Name the blood parasite species.
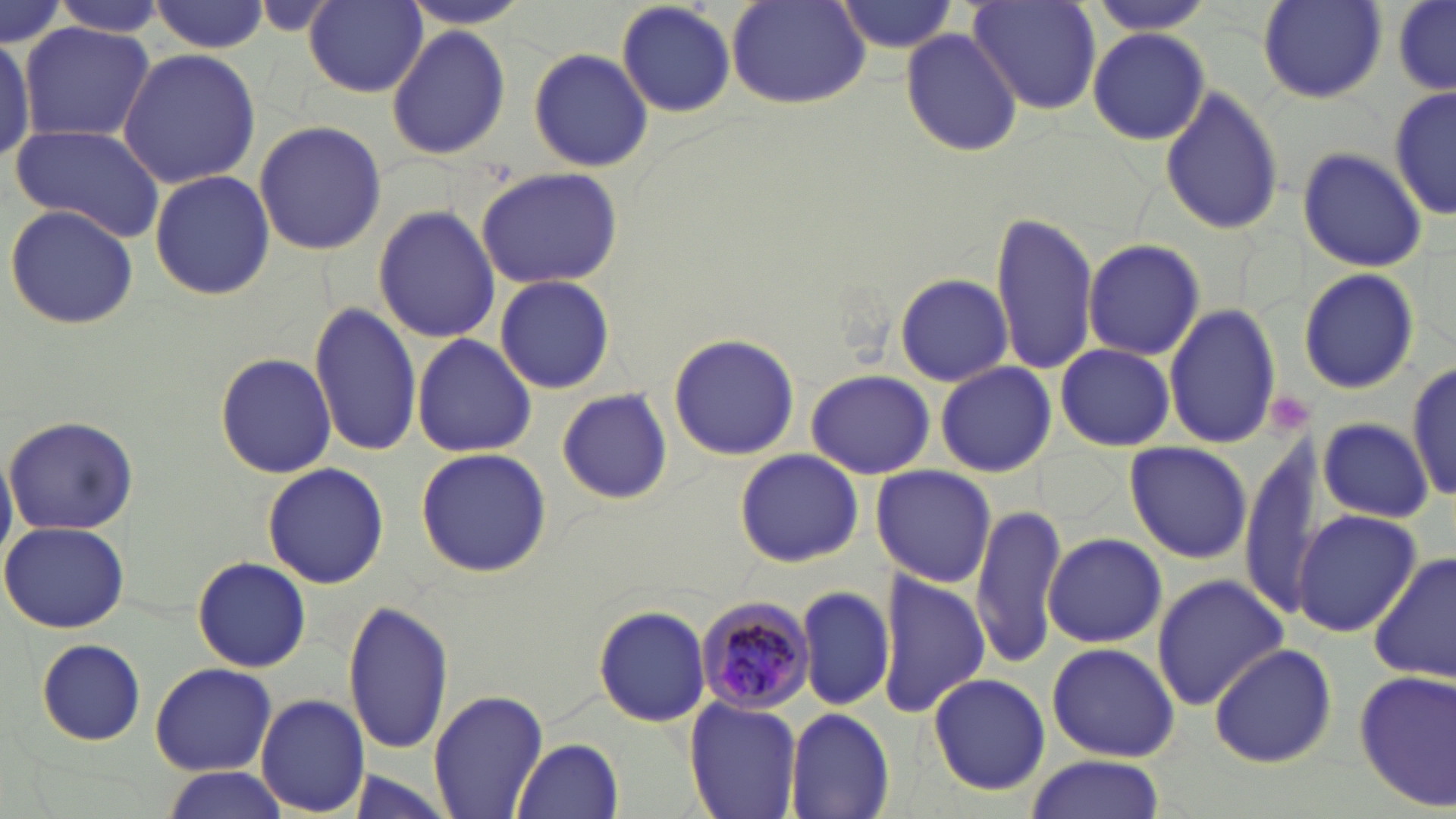
Plasmodium malariae.

Approximate bounding boxes as (x1,y1)-(x2,y2) corner pairs in pixels. Uninfected red blood cell locations: (614,0)-(738,119), (965,0)-(1101,114), (1082,0)-(1221,36), (1255,0)-(1387,104), (305,1)-(428,97), (728,1)-(872,111), (831,1)-(958,55), (1394,1)-(1456,95), (0,2)-(69,52), (147,2)-(270,54), (1390,4)-(1456,94), (19,22)-(155,142), (386,23)-(511,161), (1088,26)-(1212,147), (898,27)-(1025,158), (0,31)-(39,162), (529,46)-(657,175), (116,48)-(262,189), (1158,85)-(1285,237), (1390,85)-(1454,222), (252,118)-(387,256), (9,122)-(167,243), (1296,146)-(1428,273), (475,166)-(626,286), (150,169)-(274,301), (5,202)-(141,330), (373,204)-(497,343), (990,213)-(1099,374), (1083,240)-(1204,360), (1297,268)-(1421,394), (893,272)-(1013,386), (495,275)-(615,393), (309,300)-(420,458), (1164,303)-(1282,450), (666,331)-(802,461), (411,334)-(537,458), (1055,343)-(1175,450), (216,350)-(335,479), (1407,361)-(1454,508), (936,363)-(1057,474), (806,368)-(937,479), (555,389)-(675,507), (3,414)-(140,533), (1318,418)-(1433,522), (1242,435)-(1333,620), (1123,441)-(1252,563), (0,444)-(16,568), (734,447)-(864,568), (414,448)-(552,577), (261,462)-(389,590), (871,465)-(997,588), (971,501)-(1068,668), (1290,508)-(1421,638), (0,521)-(132,634), (1044,534)-(1167,647), (1370,551)-(1456,685), (193,556)-(310,673), (876,569)-(989,718), (1152,573)-(1288,709), (798,584)-(896,714), (342,596)-(454,756), (591,604)-(711,726), (35,638)-(146,746), (1208,641)-(1339,768), (1047,642)-(1179,760), (150,662)-(277,775), (1352,668)-(1456,810), (927,673)-(1050,793), (429,690)-(548,818), (257,694)-(370,814), (684,698)-(803,819), (785,708)-(894,819), (514,737)-(623,818), (1024,757)-(1167,819), (158,767)-(291,819). Platelet locations: (1269,393)-(1312,433). Plasmodium malariae-infected red blood cell locations: (694,592)-(814,714). Light microscopy. One field of a larger specimen. 1000x magnification. Image is 1456×819 pixels. Thin blood film. May-Grünwald-Giemsa stain.